Report the malaria status of this cell.
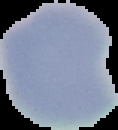
It is uninfected.

Summary:
  - Image size: 118×130 pixels
  - Preparation: thin blood smear
  - Image type: segmented cell region on a black background